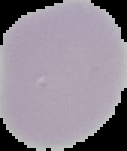
image type = cell region segmented out of the field of view; surrounding area masked to black
image size = 127×151 pixels
malaria status = uninfected
preparation = thin blood smear